Describe the morphology of the erythrocytes.
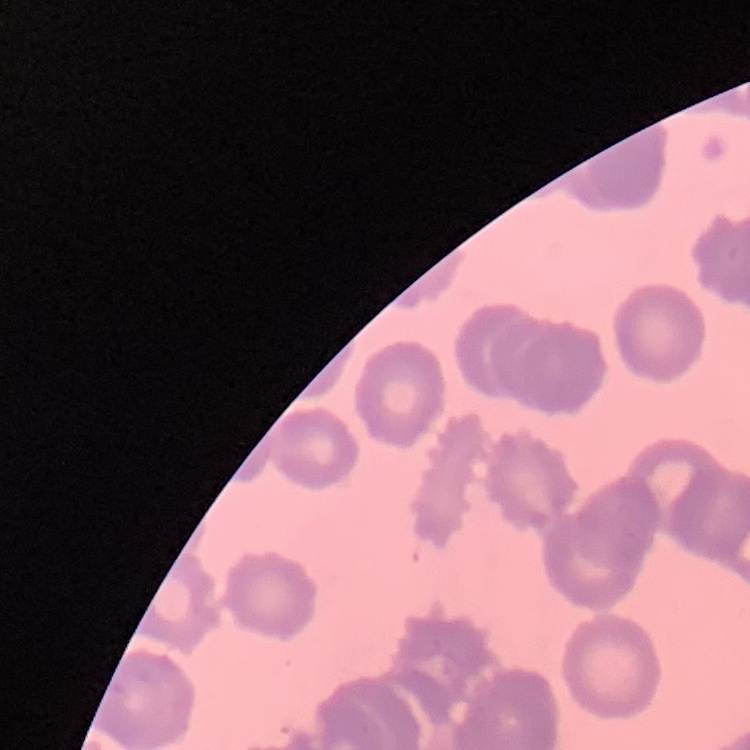
They show rouleaux formation.

Thin blood smear. Stained with either Field's or Giemsa. One tile cut from a larger photomicrograph.